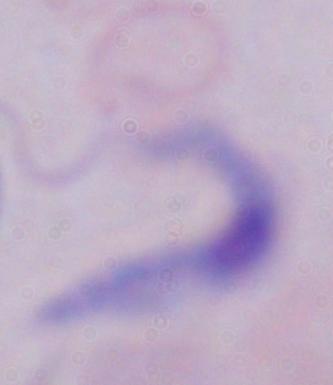

{
  "modality": "photomicrograph",
  "identification": "trypanosome",
  "magnification": "1000x"
}